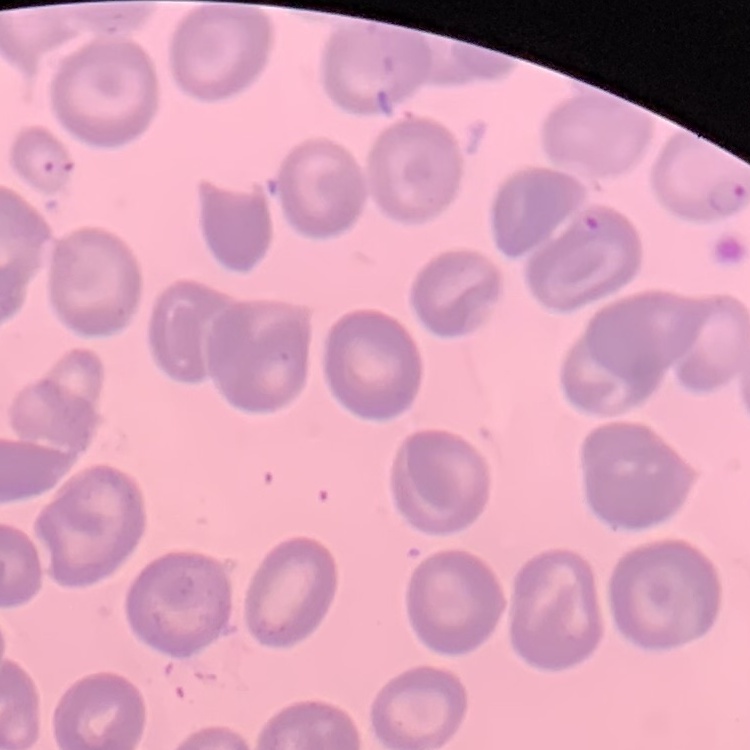

Summary:
  - Erythrocyte morphology: no rouleaux formation
  - Preparation: thin blood film
  - Stain: Field's or Giemsa
  - Image type: one tile cut from a larger photomicrograph